Find the red blood cells that are infected with Plasmodium falciparum, and any of indeterminate infection status.
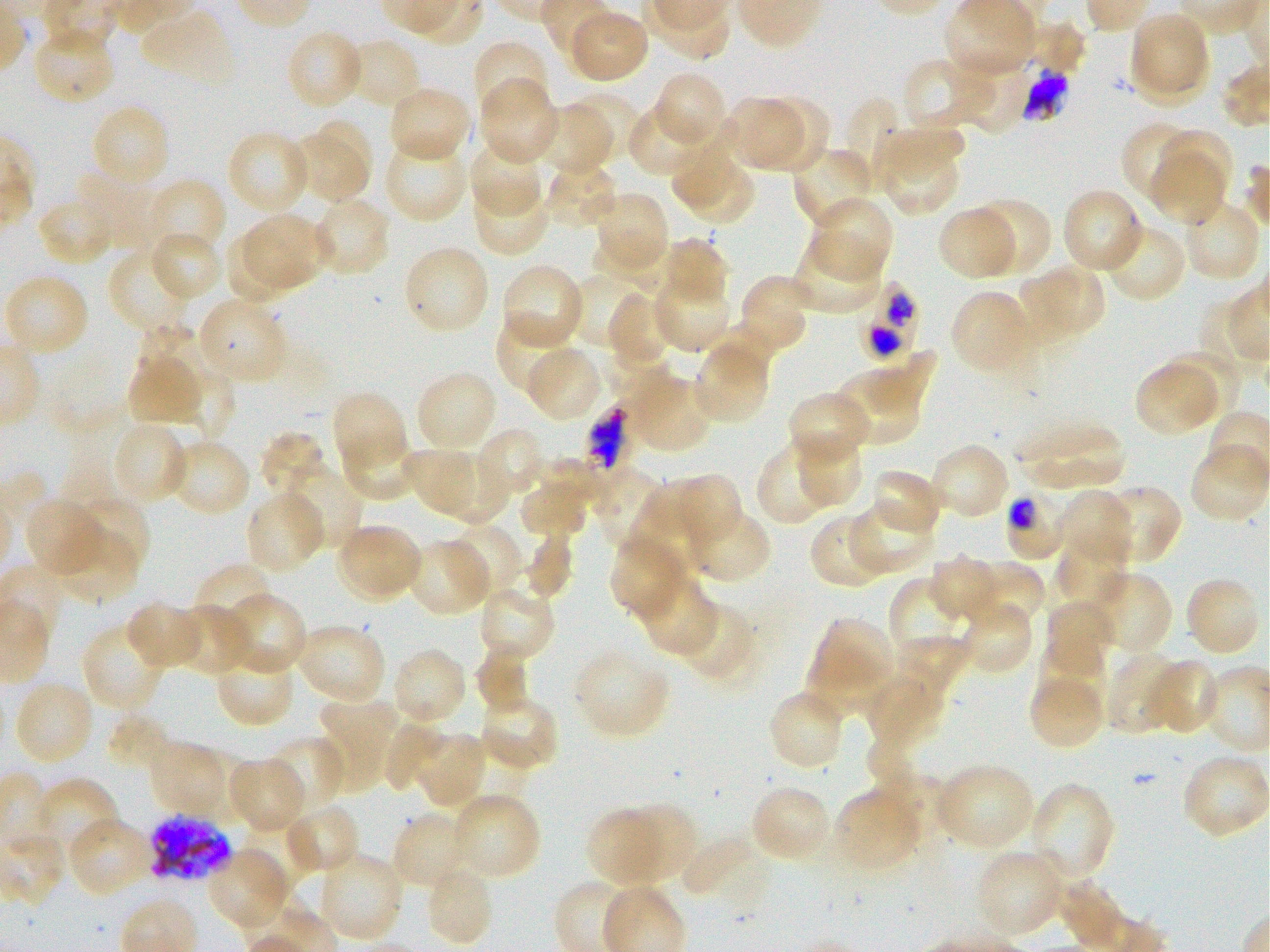
Approximate bounding boxes as (x1, y1, x2, y2) in pixels. Not every red blood cell is marked.
Infected red blood cells: (861, 281, 918, 359), (1005, 492, 1069, 561), (147, 813, 233, 883).
Red blood cells of indeterminate infection status: (1021, 67, 1070, 119), (586, 404, 627, 474).

Locations of uninfected red blood cells: (941, 1, 1035, 78), (568, 8, 650, 84), (139, 9, 235, 87), (1130, 13, 1205, 89), (1026, 20, 1088, 76), (30, 26, 116, 105), (284, 28, 365, 111), (346, 37, 421, 111), (472, 40, 550, 119), (1133, 42, 1211, 109), (957, 54, 1036, 133), (903, 57, 996, 131), (653, 72, 727, 147), (478, 80, 558, 165), (388, 86, 472, 164), (565, 91, 642, 165), (758, 96, 832, 172), (724, 97, 802, 171), (846, 97, 897, 191), (90, 103, 171, 188), (536, 103, 614, 177), (627, 103, 708, 177), (670, 117, 740, 209), (1122, 120, 1199, 205), (318, 121, 373, 179), (885, 126, 964, 186), (1160, 127, 1234, 203), (226, 130, 311, 214), (287, 135, 367, 201), (384, 136, 468, 223), (879, 140, 958, 216), (468, 142, 544, 218), (792, 146, 875, 230), (1148, 150, 1227, 226), (545, 159, 618, 229), (691, 165, 753, 222), (73, 169, 161, 250), (144, 178, 227, 261), (472, 183, 551, 257), (1061, 188, 1145, 273), (37, 195, 115, 267), (598, 195, 669, 269), (312, 196, 392, 278), (809, 196, 894, 280), (970, 196, 1052, 277), (1183, 201, 1263, 283), (937, 207, 1017, 281), (244, 214, 334, 289), (1104, 222, 1187, 304), (223, 229, 295, 304), (150, 230, 222, 301), (592, 234, 668, 297), (790, 235, 883, 316), (659, 236, 729, 309), (107, 250, 195, 333), (406, 250, 487, 331), (501, 262, 589, 348), (1039, 264, 1105, 333), (570, 271, 646, 350), (1018, 272, 1081, 347), (4, 273, 91, 357), (738, 274, 813, 353), (653, 277, 732, 352), (950, 290, 1030, 373), (607, 292, 668, 361), (200, 297, 288, 382), (495, 316, 579, 395), (139, 323, 200, 402), (701, 334, 773, 383), (694, 344, 771, 423), (524, 346, 603, 423), (1164, 347, 1244, 420), (861, 348, 936, 414), (601, 349, 672, 399), (128, 357, 202, 427), (1135, 362, 1218, 437), (173, 368, 236, 445), (833, 370, 920, 445), (628, 372, 713, 452), (418, 374, 492, 449), (787, 389, 869, 466), (332, 391, 408, 472), (1017, 421, 1126, 491), (112, 422, 190, 505), (476, 428, 546, 501), (341, 429, 417, 503), (258, 431, 326, 499), (797, 433, 860, 505), (167, 439, 251, 519), (929, 442, 1010, 521), (757, 443, 833, 524), (399, 447, 477, 512), (428, 454, 510, 525), (536, 459, 610, 502), (600, 466, 669, 550), (870, 467, 943, 537), (279, 468, 361, 553), (659, 474, 743, 546), (518, 476, 591, 539), (1103, 484, 1181, 558), (1056, 489, 1133, 568), (244, 491, 325, 574), (65, 493, 150, 573), (24, 497, 105, 578), (628, 498, 708, 582), (847, 503, 935, 575), (690, 508, 772, 584), (809, 513, 884, 590), (442, 523, 523, 599), (336, 524, 423, 602), (56, 528, 138, 605), (520, 533, 574, 602), (610, 535, 685, 619), (408, 538, 490, 617), (1058, 539, 1127, 612), (928, 554, 999, 622), (968, 560, 1045, 630), (194, 563, 278, 630), (1088, 571, 1172, 655), (635, 573, 716, 656), (889, 576, 957, 652), (1189, 582, 1258, 652), (478, 583, 558, 664), (221, 593, 306, 676), (1043, 598, 1115, 670), (126, 600, 203, 671), (959, 600, 1035, 675), (677, 602, 758, 685), (177, 604, 252, 678), (812, 617, 894, 690), (294, 621, 388, 704), (80, 622, 165, 715), (895, 634, 973, 694), (1035, 640, 1107, 708), (214, 644, 295, 728), (391, 647, 468, 727), (475, 647, 536, 716), (574, 649, 671, 738), (805, 651, 882, 718), (1105, 651, 1181, 736), (1146, 658, 1220, 737), (863, 676, 945, 748), (1030, 677, 1102, 745), (13, 680, 95, 766), (478, 693, 559, 772), (317, 695, 398, 792), (771, 696, 843, 765), (106, 712, 174, 772), (380, 719, 445, 792), (412, 731, 487, 809), (269, 735, 345, 814), (864, 737, 918, 790), (147, 741, 223, 817), (190, 751, 256, 828), (1181, 754, 1270, 839), (228, 757, 307, 834), (935, 763, 1035, 851), (873, 770, 948, 838), (35, 777, 120, 862), (1029, 784, 1114, 882), (750, 785, 830, 863), (836, 790, 919, 867), (450, 792, 542, 880), (282, 803, 361, 877), (616, 804, 694, 883), (243, 809, 318, 890), (585, 809, 664, 887), (391, 811, 470, 890), (66, 817, 155, 898), (681, 835, 766, 905), (205, 847, 291, 931), (974, 849, 1066, 939), (317, 852, 405, 944), (425, 863, 496, 947), (1058, 881, 1128, 949). 100x oil-immersion objective, numerical aperture 1.25. Single field of view. Thin blood smear. Plasmodium falciparum strain 3D7 maintained in static in-vitro culture. Image is 1270×952 pixels. Giemsa stain. Donor blood group O+.